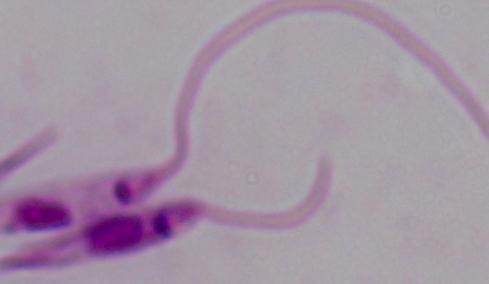
Summary:
  - Magnification: 1000x
  - Identification: Leishmania
  - Modality: photomicrograph